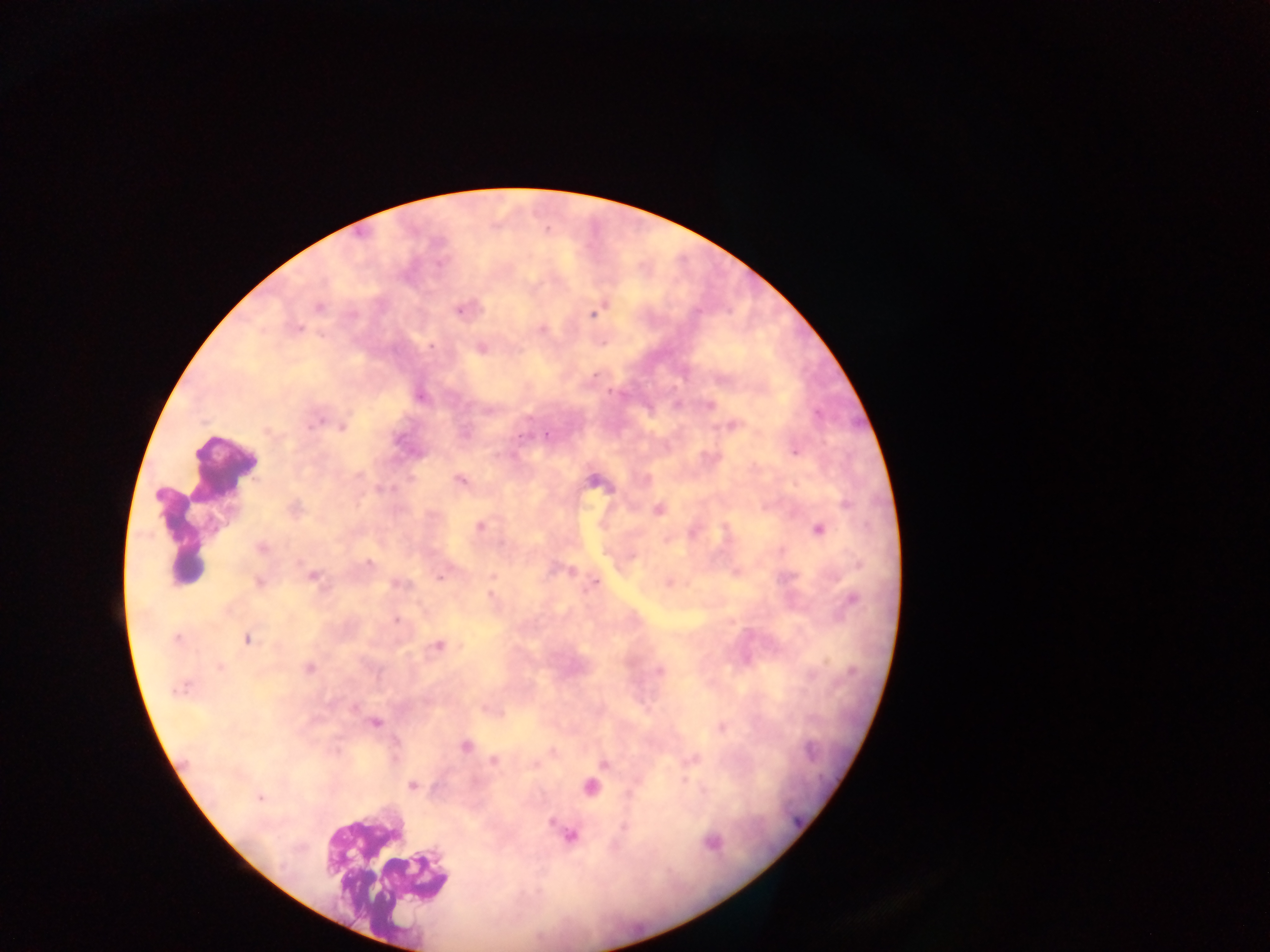

field_of_view: single
preparation: thick blood film
leukocyte_locations: 'approximate centers as [x, y] in pixels: [229, 471], [177, 536], [386, 875]'
country: Ghana
capture: mobile-phone photograph through a microscope
image_size: 1270×952 pixels
malaria_parasite_locations: 'approximate centers as [x, y] in pixels: [459, 310], [590, 313], [297, 327], [432, 345], [266, 430], [795, 451], [459, 479], [480, 527], [369, 562], [439, 577], [314, 578], [395, 584], [395, 620], [438, 645], [219, 667], [308, 668], [183, 693], [354, 709], [377, 724], [395, 744], [465, 745], [393, 753], [412, 786], [258, 799]'